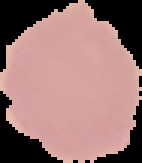
image type = segmented cell region on a black background
malaria status = uninfected
image size = 142×163 pixels
preparation = thin blood film